Assess this cell for malaria.
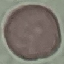
It is uninfected.

Summary:
  - Stain: Giemsa
  - Preparation: thin smear
  - Capture: smartphone through the microscope eyepiece
  - Image type: cell patch, automatically extracted from a larger field of view and resized to 64 × 64 pixels